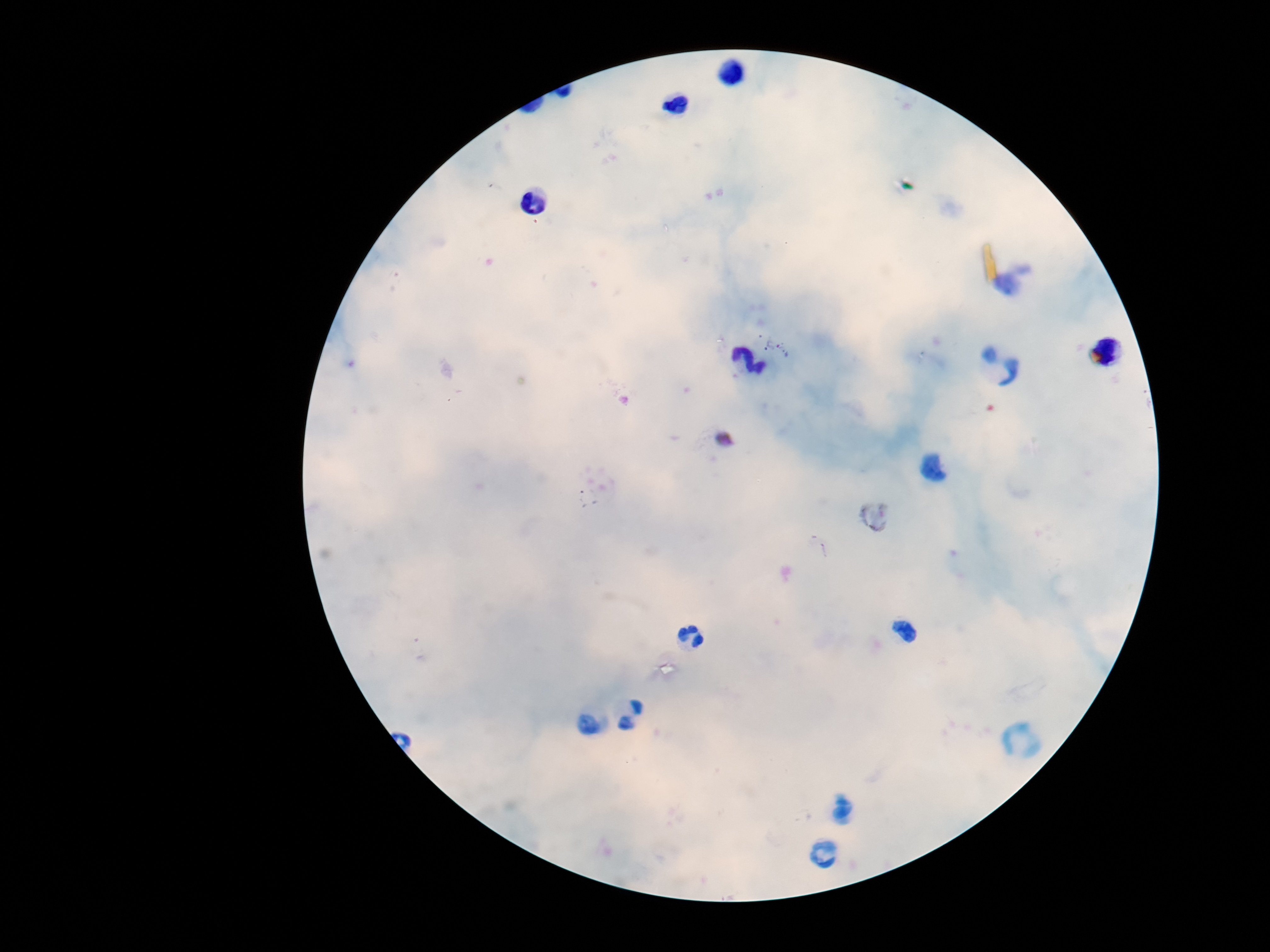

field of view = single
image size = 1270×952 pixels
capture = smartphone camera through the microscope eyepiece
preparation = thick blood film
Plasmodium parasite locations = approximate centers as [x, y] in pixels: [776, 342]
patient malaria status = positive
stain = Giemsa
magnification = 100x